Give the preparation type.
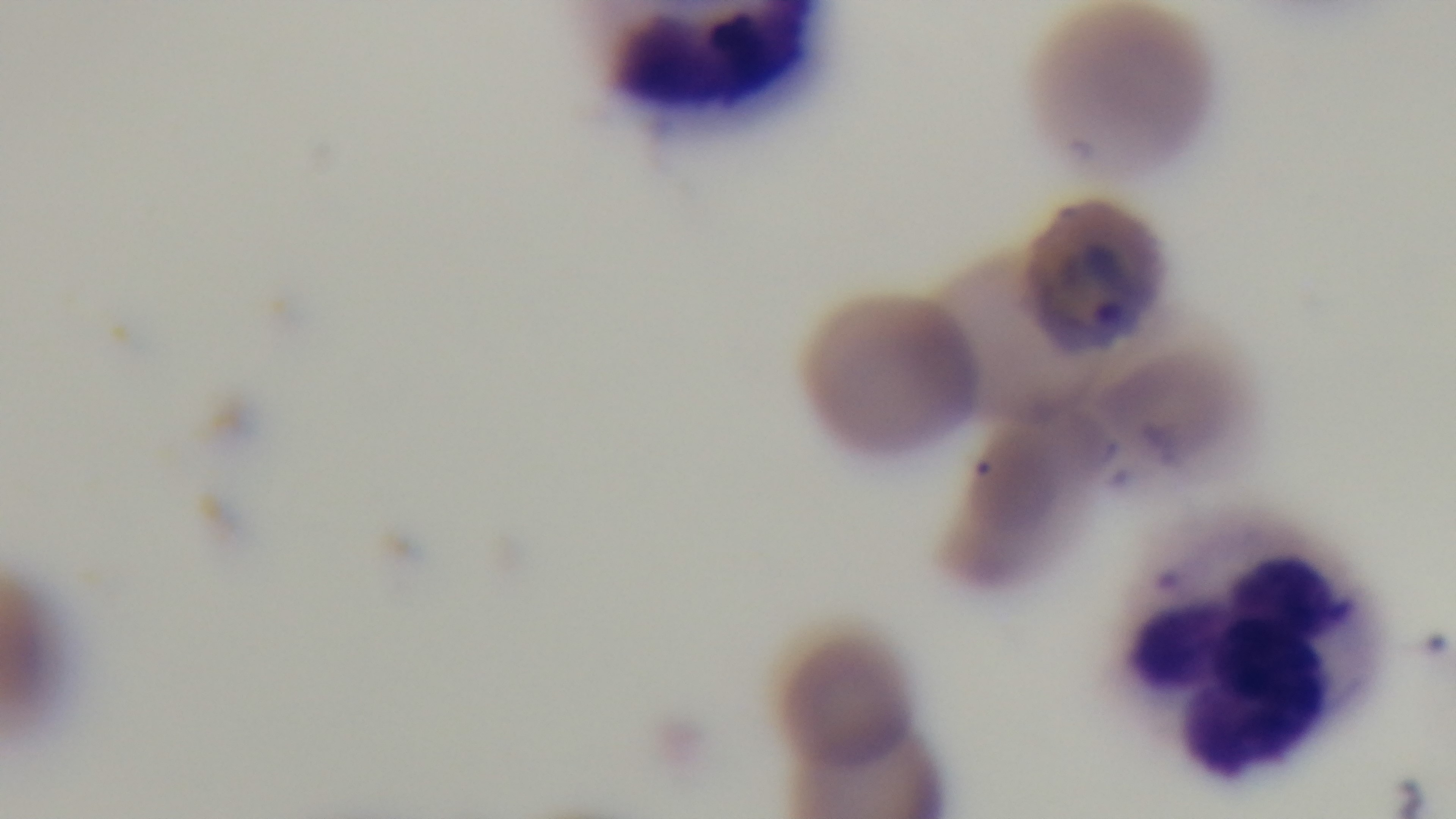

It is a thin blood film.

objective: 100x oil immersion
capture: mounted 4K digital camera
modality: light microscopy
malaria_status: positive
field_of_view: single
stain: Giemsa